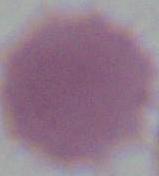

magnification: 1000x
identification: erythrocyte
modality: micrograph